Classify this cell by malaria status.
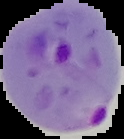

It is parasitized.

Summary:
  - Image type: segmented cell region with the area outside set to black
  - Image size: 124×139 pixels
  - Preparation: thin blood smear